Assess the morphology of the red blood cells.
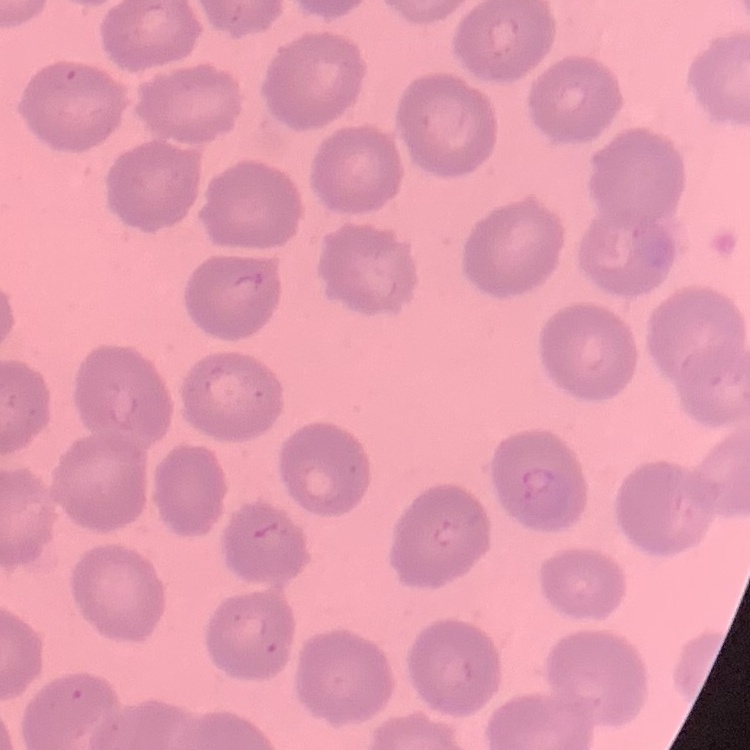

No rouleaux formation.

Summary:
  - Stain: Field's or Giemsa
  - Image type: square crop of a larger photomicrograph
  - Preparation: thin peripheral smear